Assess the morphology of the erythrocytes.
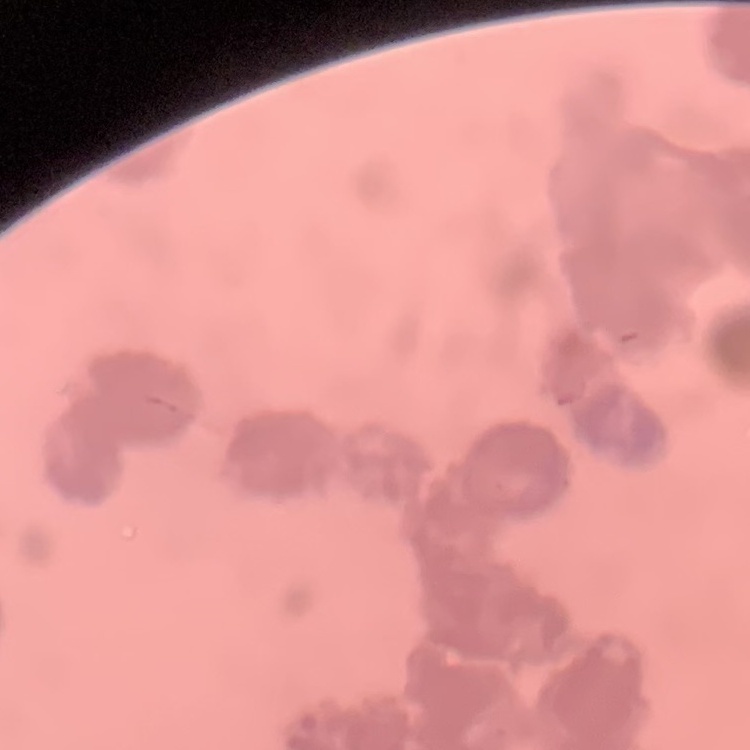

They show rouleaux formation.

Stained with either Field's or Giemsa. Square crop of a larger photomicrograph. Thin blood film.